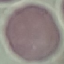
Result: no malaria parasites detected. Cell patch, automatically extracted from a larger field of view and resized to 64 × 64 pixels. Photographed with a smartphone camera at the microscope eyepiece. Giemsa-stained preparation. Thin smear of blood.